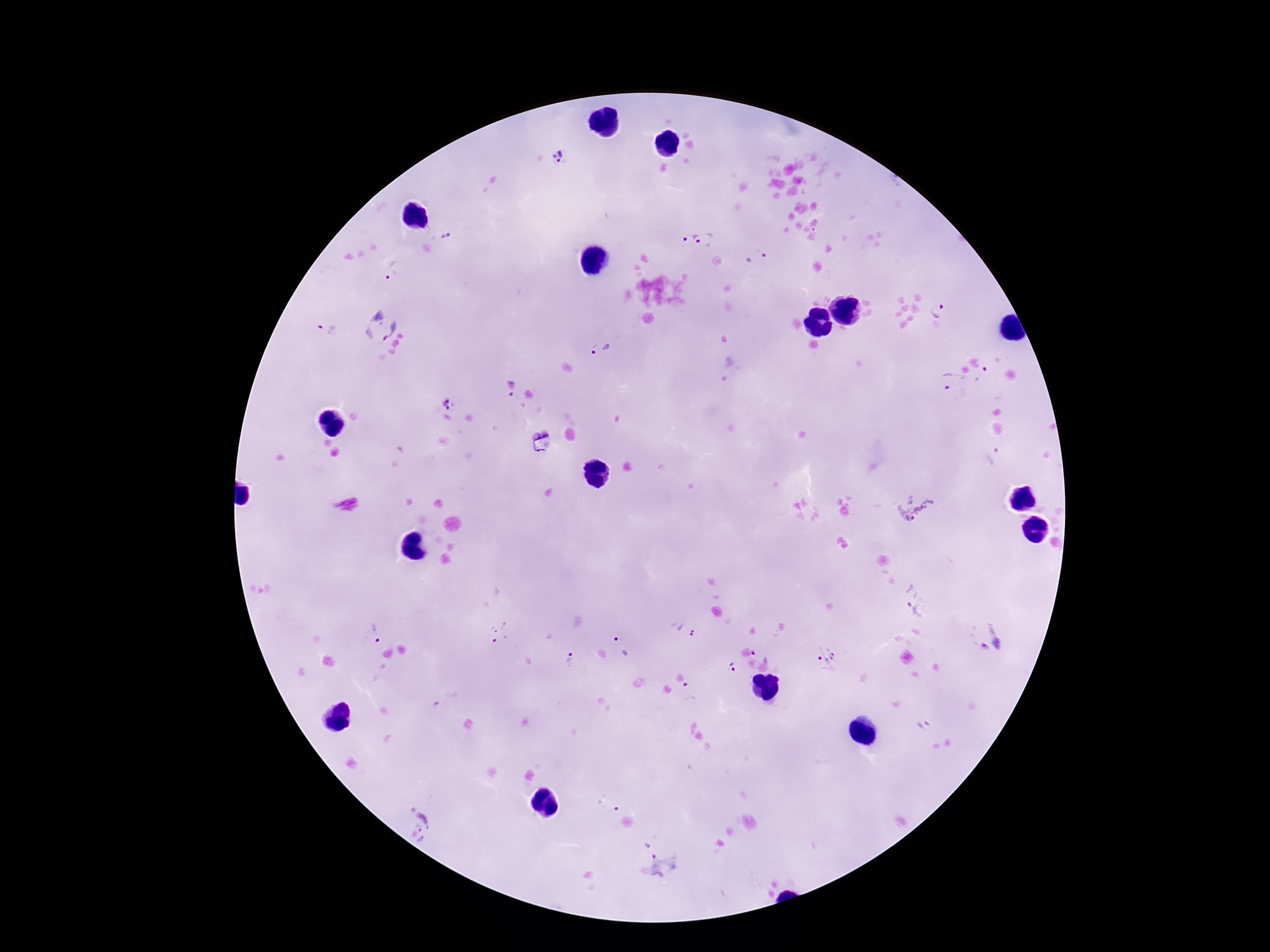 Approximate centers as (x, y) in pixels. Plasmodium parasite locations: (559, 160), (446, 235), (696, 241), (757, 257), (391, 271), (938, 311), (380, 326), (329, 330), (601, 350), (982, 376), (952, 381), (512, 389), (449, 403), (916, 508), (917, 604), (685, 628), (502, 632), (378, 633), (992, 638), (622, 645), (763, 649), (827, 656), (571, 657), (733, 667), (690, 692), (446, 699), (924, 725), (607, 802), (421, 825), (663, 867). Single field of view. 100x magnification. Giemsa-stained preparation. Patient malaria status: positive. Smartphone photograph taken through the microscope eyepiece. Image is 1270×952 pixels. Thick peripheral-blood smear.